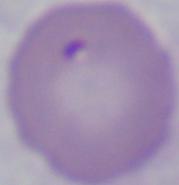
Micrograph. 1000x magnification. A Babesia parasite is shown.